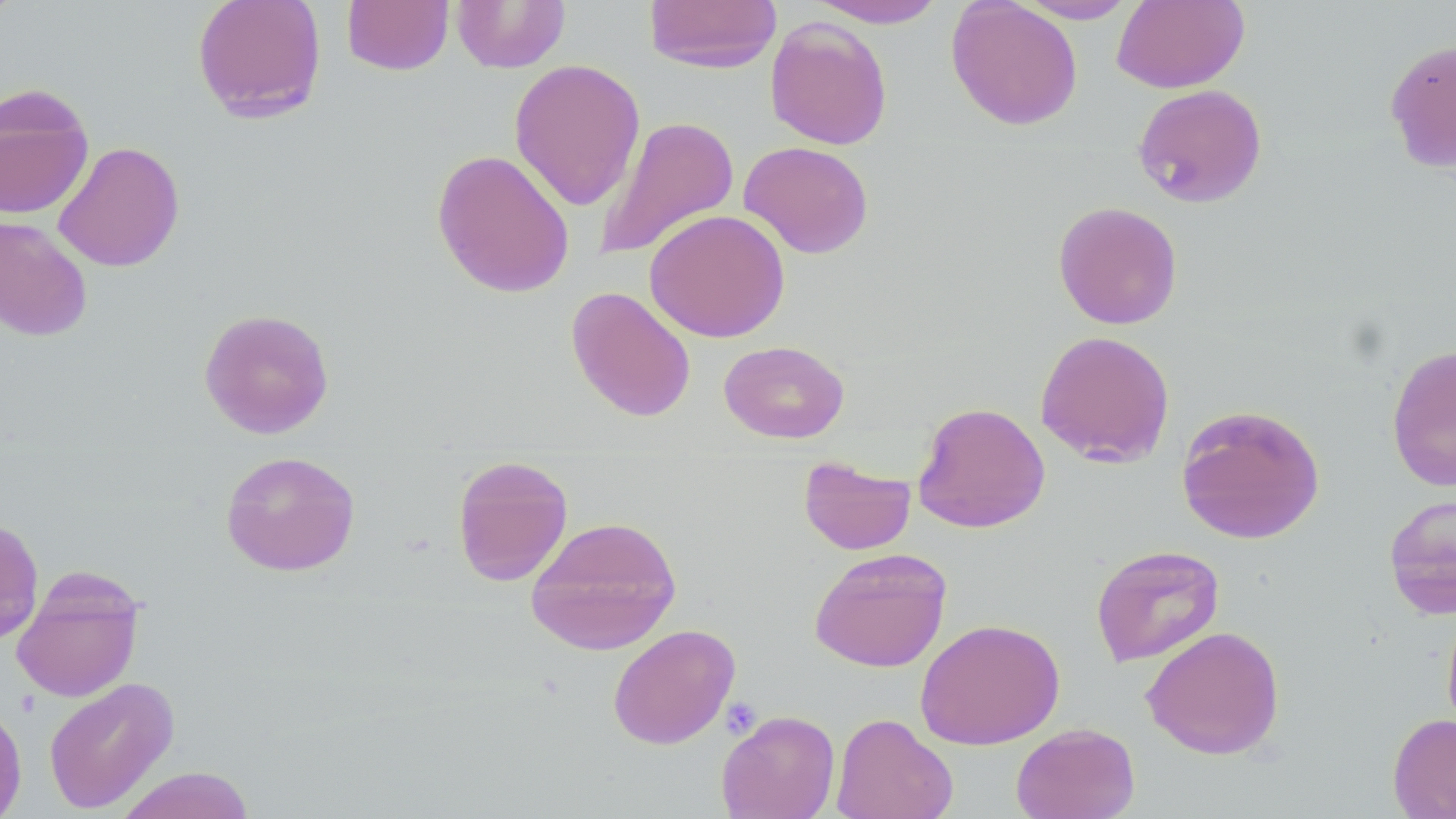

slide-level diagnosis = negative for blood parasites
preparation = thin blood film
image size = 1456×819 pixels
field of view = one of a larger specimen
stain = May-Grünwald-Giemsa
modality = light microscopy
magnification = 1000x
uninfected red blood cell locations = approximate bounding boxes as (x1, y1, x2, y2) in pixels: (644, 0, 782, 73), (805, 0, 950, 28), (946, 0, 1083, 131), (1012, 0, 1139, 23), (1112, 0, 1250, 93), (191, 1, 328, 123), (342, 1, 454, 75), (451, 1, 570, 72), (765, 17, 893, 150), (1383, 36, 1456, 176), (508, 58, 646, 211), (1132, 84, 1268, 209), (0, 85, 94, 220), (594, 115, 739, 262), (53, 140, 185, 272), (738, 140, 874, 259), (432, 148, 575, 299), (1053, 201, 1183, 329), (644, 209, 790, 343), (0, 215, 93, 342), (566, 286, 696, 423), (198, 307, 335, 439), (1034, 330, 1176, 468), (718, 339, 849, 444), (1386, 343, 1456, 492), (912, 402, 1051, 533), (1176, 404, 1326, 546), (219, 450, 361, 577), (452, 455, 573, 587), (798, 456, 916, 555), (1382, 493, 1456, 620), (0, 514, 45, 647), (525, 515, 683, 656), (1090, 544, 1225, 667), (809, 547, 952, 673), (11, 568, 146, 702), (1441, 606, 1456, 742), (915, 618, 1065, 750), (607, 623, 740, 750), (1141, 625, 1286, 760), (42, 676, 179, 813), (0, 698, 28, 819), (716, 709, 840, 819), (831, 712, 958, 819), (1387, 713, 1456, 818), (1010, 722, 1141, 819), (115, 766, 255, 819)